Report the malaria status of this cell.
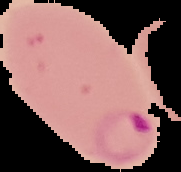
It is parasitized.

From a thin blood smear. Image is 181×172 pixels. Segmented cell region on a black background.